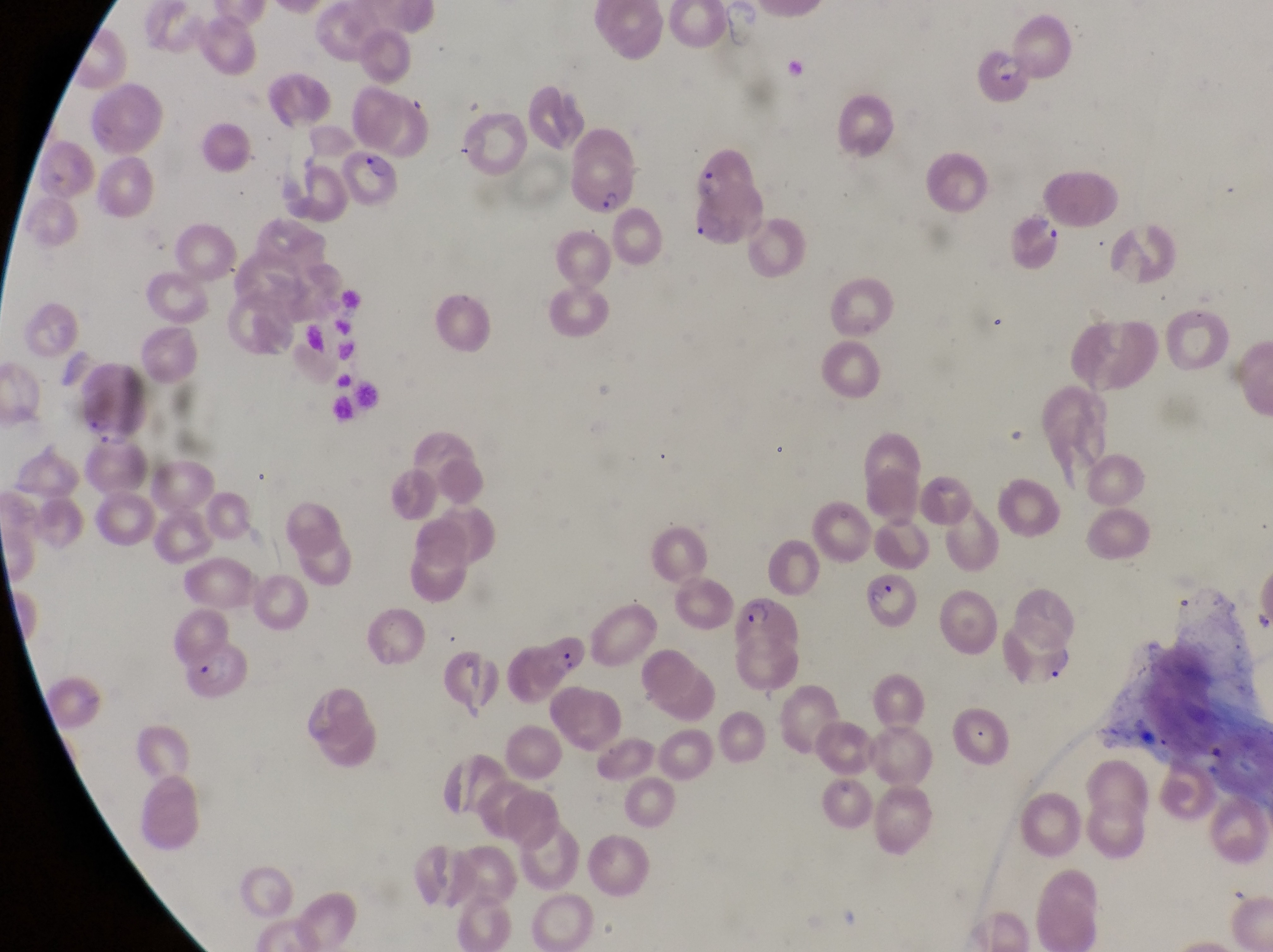

Approximate bounding boxes as {left, top, right, bottom} in pixels. Parasitised red blood cell locations: {976, 50, 1036, 113}, {342, 143, 404, 211}, {692, 147, 763, 244}, {565, 152, 637, 219}, {1011, 211, 1062, 264}, {72, 360, 147, 450}, {866, 568, 919, 633}, {734, 594, 806, 657}, {190, 647, 260, 707}. Thin blood film. Single field of view. Image is 1273×952 pixels. Sample from Uganda. Magnification of 1000x. Photographed through the eyepiece of an Olympus CX-23 microscope with a smartphone camera.